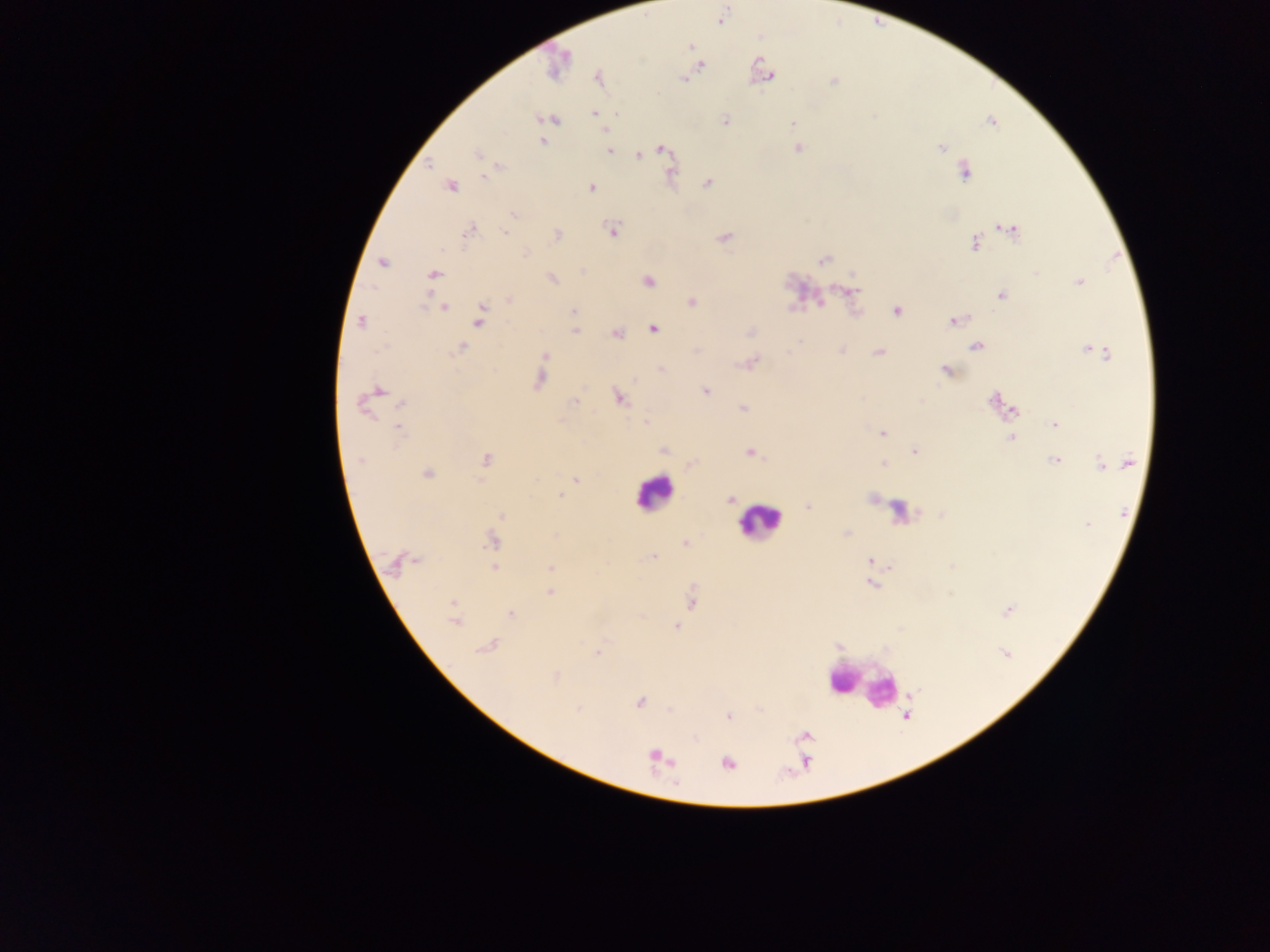
Approximate centers as {x, y} in pixels.
Summary:
  - Plasmodium parasite locations: {719, 22}, {693, 47}, {567, 56}, {702, 66}, {770, 76}, {684, 79}, {833, 82}, {595, 114}, {874, 118}, {540, 119}, {556, 120}, {724, 120}, {991, 122}, {791, 123}, {543, 140}, {659, 148}, {798, 148}, {941, 149}, {610, 151}, {637, 154}, {431, 163}, {962, 169}, {483, 177}, {706, 183}, {592, 187}, {513, 214}, {1000, 226}, {1015, 228}, {612, 229}, {469, 230}, {504, 234}, {723, 238}, {973, 243}, {527, 254}, {824, 259}, {1037, 271}, {647, 280}, {1078, 281}, {847, 288}, {1000, 295}, {508, 300}, {691, 301}, {821, 302}, {793, 307}, {445, 308}, {575, 310}, {896, 312}, {951, 322}, {575, 329}, {654, 329}, {750, 331}, {617, 335}, {973, 345}, {1093, 346}, {462, 347}, {695, 350}, {840, 350}, {879, 353}, {660, 369}, {946, 371}, {705, 391}, {994, 397}, {618, 398}, {575, 401}, {402, 403}, {741, 408}, {1011, 411}, {1053, 422}, {399, 427}, {882, 433}, {663, 449}, {913, 451}, {749, 452}, {485, 458}, {1059, 458}, {360, 460}, {1127, 462}, {1099, 463}, {690, 464}, {576, 479}, {558, 495}, {731, 500}, {807, 507}, {1087, 526}, {686, 543}, {654, 557}, {416, 559}, {867, 559}, {550, 566}, {890, 567}, {870, 584}, {550, 593}, {692, 603}, {1008, 611}, {512, 615}, {676, 626}, {597, 654}, {641, 701}, {728, 717}, {671, 762}
  - Leukocyte locations: {652, 498}, {757, 523}, {859, 688}
  - Preparation: thick blood film
  - Capture: mobile-phone photograph through a microscope
  - Image size: 1270×952 pixels
  - Field of view: single
  - Country: Ghana